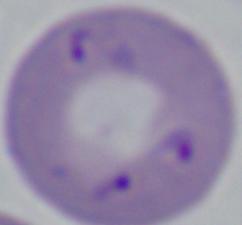 A Babesia parasite is seen. Captured at 1000x magnification. Photomicrograph.